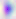

Summary:
  - Magnification: 400x
  - Modality: photomicrograph
  - Identification: Toxoplasma gondii